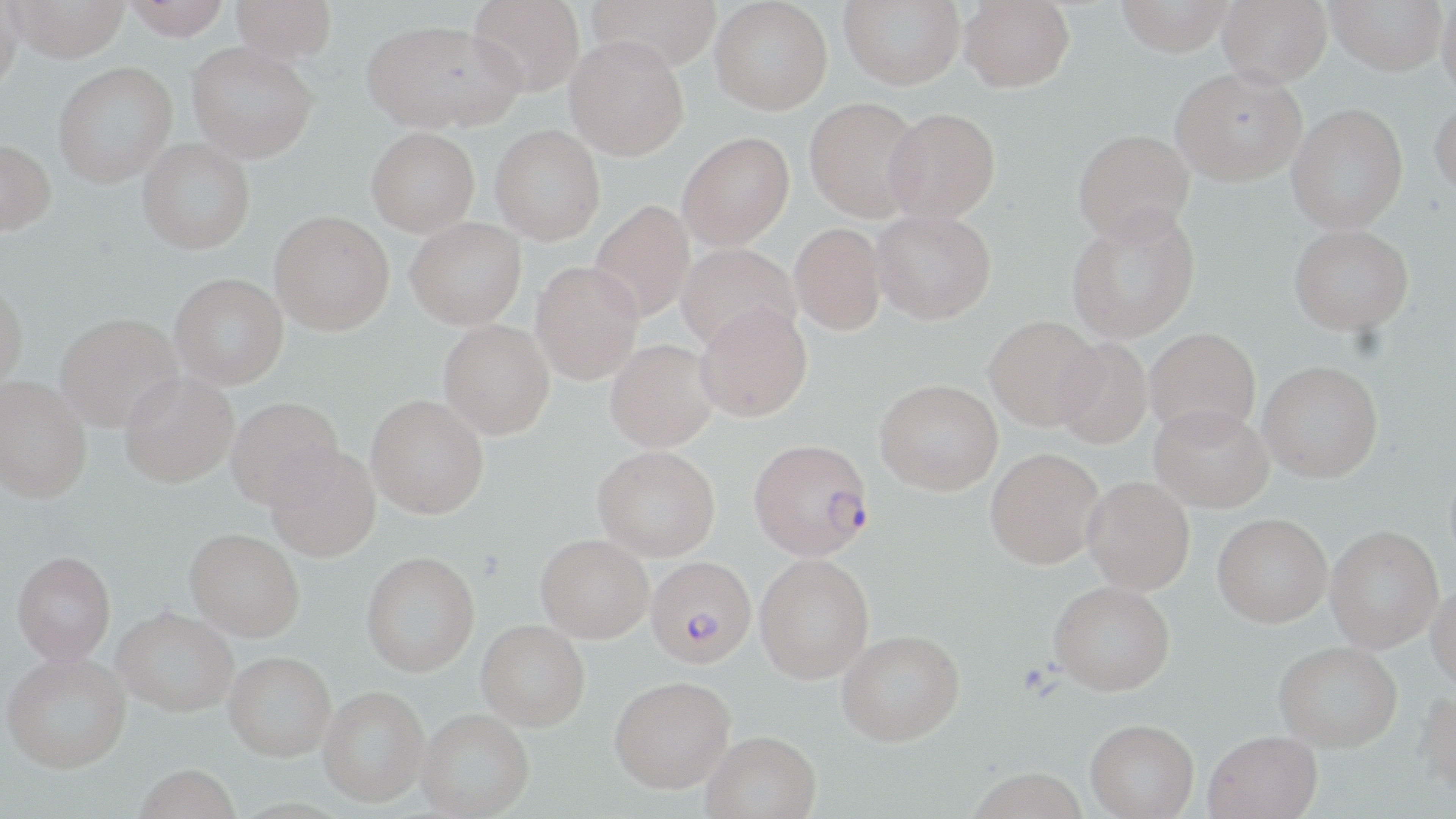

Approximate bounding boxes as (x1, y1, x2, y2) in pixels. Plasmodium falciparum-infected red blood cell locations: (749, 444, 873, 562), (646, 558, 755, 669). Uninfected red blood cell locations: (122, 0, 231, 40), (230, 0, 337, 64), (468, 0, 585, 96), (587, 0, 722, 73), (710, 0, 833, 115), (839, 0, 965, 90), (959, 0, 1074, 92), (1116, 0, 1233, 56), (1216, 0, 1332, 87), (1327, 0, 1448, 75), (0, 1, 25, 91), (9, 1, 129, 63), (1436, 2, 1456, 99), (362, 19, 519, 133), (564, 36, 689, 160), (187, 41, 317, 163), (52, 62, 177, 188), (1171, 66, 1307, 186), (804, 97, 924, 222), (1429, 97, 1456, 201), (1286, 103, 1408, 234), (883, 107, 1000, 223), (490, 124, 605, 245), (366, 127, 479, 236), (1072, 128, 1194, 244), (677, 131, 794, 250), (0, 138, 56, 236), (137, 138, 254, 255), (589, 200, 695, 323), (1066, 207, 1199, 343), (871, 209, 996, 324), (269, 210, 394, 335), (405, 217, 526, 329), (789, 223, 887, 335), (1289, 224, 1413, 335), (676, 242, 801, 354), (530, 261, 644, 384), (169, 272, 288, 389), (0, 281, 28, 394), (695, 301, 812, 423), (54, 311, 183, 431), (984, 315, 1103, 431), (438, 319, 555, 440), (1144, 327, 1261, 441), (1052, 337, 1152, 450), (605, 339, 719, 453), (1257, 360, 1383, 483), (119, 371, 237, 488), (0, 375, 92, 505), (875, 378, 1003, 495), (366, 394, 489, 520), (226, 397, 343, 512), (1149, 404, 1273, 512), (264, 447, 382, 564), (592, 447, 719, 563), (985, 447, 1104, 569), (1081, 476, 1195, 595), (1211, 513, 1331, 628), (1325, 526, 1442, 652), (184, 531, 304, 643), (535, 537, 653, 646), (11, 551, 116, 666), (361, 553, 480, 679), (754, 554, 874, 683), (1048, 581, 1175, 696), (1426, 582, 1456, 696), (113, 610, 238, 721), (476, 622, 590, 734), (836, 630, 965, 748), (1274, 644, 1401, 756), (224, 654, 337, 766), (2, 655, 132, 779), (609, 681, 735, 799), (317, 688, 428, 811), (1410, 693, 1456, 802), (416, 712, 534, 819), (1085, 723, 1199, 819), (702, 734, 821, 819), (1202, 734, 1323, 819), (133, 768, 241, 819), (965, 769, 1090, 819). Slide-level diagnosis: Plasmodium falciparum. Optical microscopy. Image is 1456×819 pixels. May-Grünwald-Giemsa stain. 1000x magnification. Thin blood film. One field of a larger specimen.